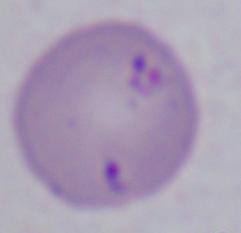 1000x magnification. A Babesia parasite is seen. Photomicrograph.